Identify the blood parasite species.
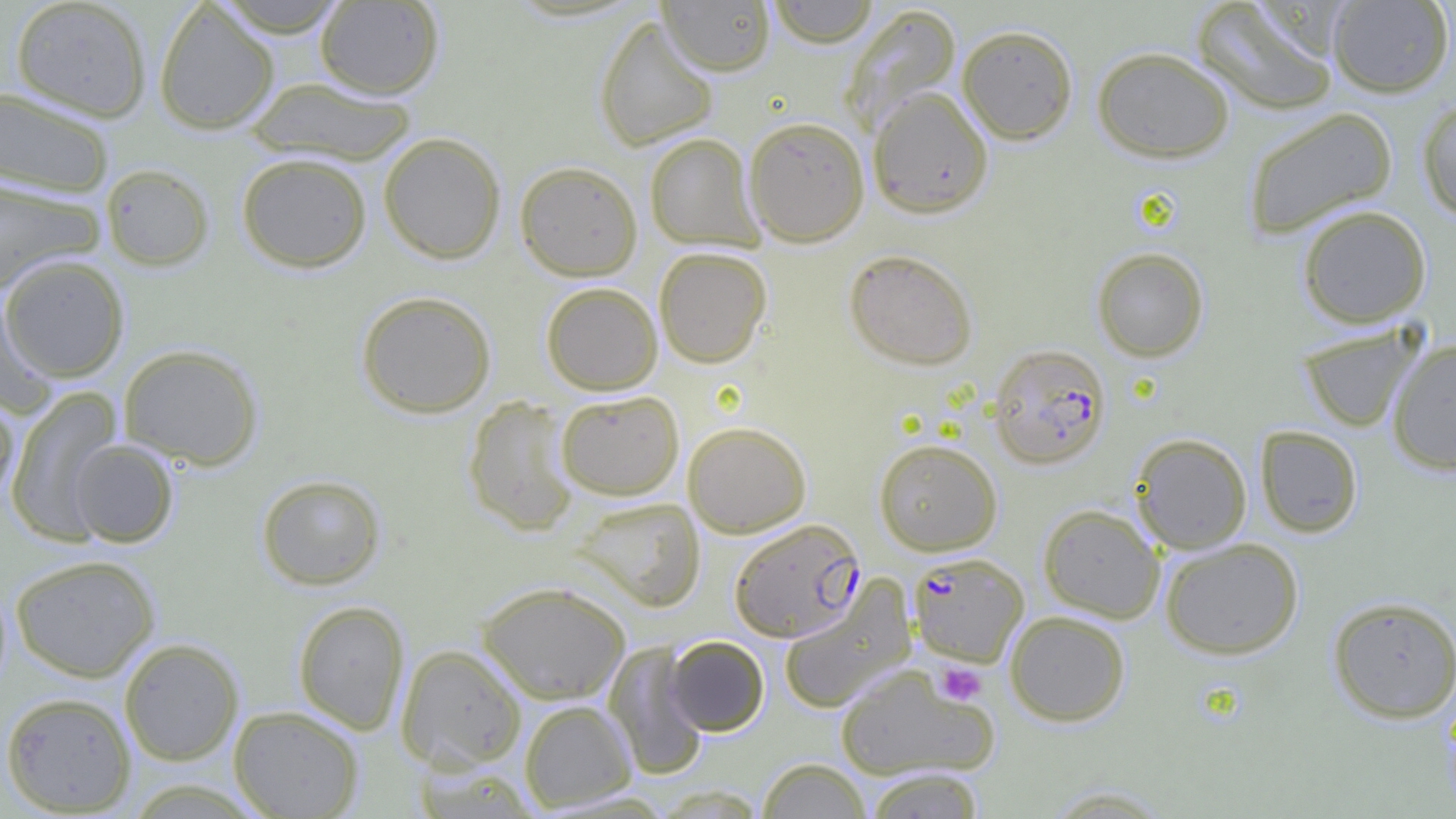
Plasmodium falciparum.

field of view = single
Plasmodium falciparum-infected red blood cell locations = approximate bounding boxes as named x1/y1/x2/y2 corners in pixels: (x1=988, y1=343, x2=1112, y2=469), (x1=729, y1=517, x2=865, y2=642), (x1=908, y1=552, x2=1028, y2=667)
preparation = thin blood film
image size = 1456×819 pixels
platelet locations = approximate bounding boxes as named x1/y1/x2/y2 corners in pixels: (x1=935, y1=662, x2=987, y2=706)
magnification = 1000x
modality = optical microscopy
uninfected red blood cell locations = approximate bounding boxes as named x1/y1/x2/y2 corners in pixels: (x1=211, y1=0, x2=352, y2=37), (x1=658, y1=0, x2=775, y2=76), (x1=764, y1=0, x2=881, y2=47), (x1=1191, y1=0, x2=1340, y2=117), (x1=1327, y1=0, x2=1454, y2=98), (x1=10, y1=1, x2=151, y2=121), (x1=153, y1=1, x2=279, y2=135), (x1=315, y1=1, x2=444, y2=99), (x1=840, y1=5, x2=962, y2=136), (x1=593, y1=14, x2=719, y2=152), (x1=957, y1=24, x2=1078, y2=144), (x1=1091, y1=46, x2=1235, y2=163), (x1=245, y1=77, x2=418, y2=165), (x1=1, y1=86, x2=115, y2=199), (x1=867, y1=87, x2=994, y2=218), (x1=1417, y1=97, x2=1456, y2=221), (x1=1242, y1=107, x2=1398, y2=238), (x1=743, y1=116, x2=870, y2=246), (x1=378, y1=132, x2=506, y2=264), (x1=644, y1=133, x2=764, y2=251), (x1=236, y1=152, x2=372, y2=273), (x1=515, y1=161, x2=643, y2=281), (x1=101, y1=164, x2=215, y2=271), (x1=0, y1=176, x2=106, y2=291), (x1=1297, y1=205, x2=1432, y2=329), (x1=653, y1=246, x2=772, y2=368), (x1=1091, y1=247, x2=1209, y2=362), (x1=843, y1=249, x2=978, y2=370), (x1=1, y1=254, x2=130, y2=383), (x1=541, y1=282, x2=663, y2=395), (x1=0, y1=290, x2=57, y2=416), (x1=356, y1=290, x2=497, y2=418), (x1=1296, y1=322, x2=1425, y2=433), (x1=1386, y1=339, x2=1456, y2=476), (x1=118, y1=343, x2=264, y2=469), (x1=6, y1=387, x2=124, y2=544), (x1=0, y1=390, x2=19, y2=507), (x1=556, y1=390, x2=684, y2=500), (x1=463, y1=396, x2=580, y2=536), (x1=683, y1=421, x2=811, y2=538), (x1=1254, y1=425, x2=1364, y2=538), (x1=1130, y1=433, x2=1252, y2=554), (x1=874, y1=438, x2=1002, y2=556), (x1=68, y1=439, x2=179, y2=547), (x1=256, y1=473, x2=387, y2=590), (x1=571, y1=496, x2=705, y2=611), (x1=1038, y1=503, x2=1165, y2=622), (x1=1160, y1=537, x2=1304, y2=659), (x1=10, y1=553, x2=161, y2=682), (x1=778, y1=577, x2=916, y2=713), (x1=477, y1=580, x2=631, y2=704), (x1=1327, y1=595, x2=1456, y2=723), (x1=293, y1=599, x2=410, y2=734), (x1=1005, y1=610, x2=1131, y2=726), (x1=665, y1=635, x2=769, y2=736), (x1=119, y1=638, x2=244, y2=766), (x1=603, y1=642, x2=709, y2=781), (x1=396, y1=643, x2=527, y2=771), (x1=833, y1=665, x2=999, y2=782), (x1=1, y1=691, x2=137, y2=815), (x1=519, y1=699, x2=637, y2=812), (x1=228, y1=705, x2=365, y2=818), (x1=757, y1=758, x2=871, y2=819), (x1=863, y1=767, x2=987, y2=818), (x1=1039, y1=784, x2=1177, y2=818)